Assess the morphology of the red blood cells.
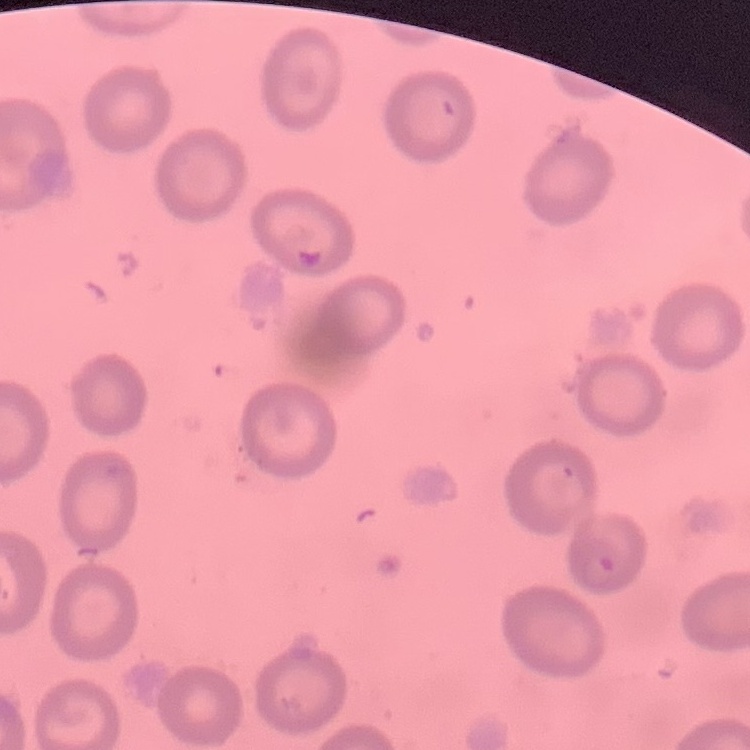

They show no rouleaux formation.

Thin blood smear. Stained with either Field's or Giemsa. One tile cut from a larger photomicrograph.